Locate every blood parasite and identify its species.
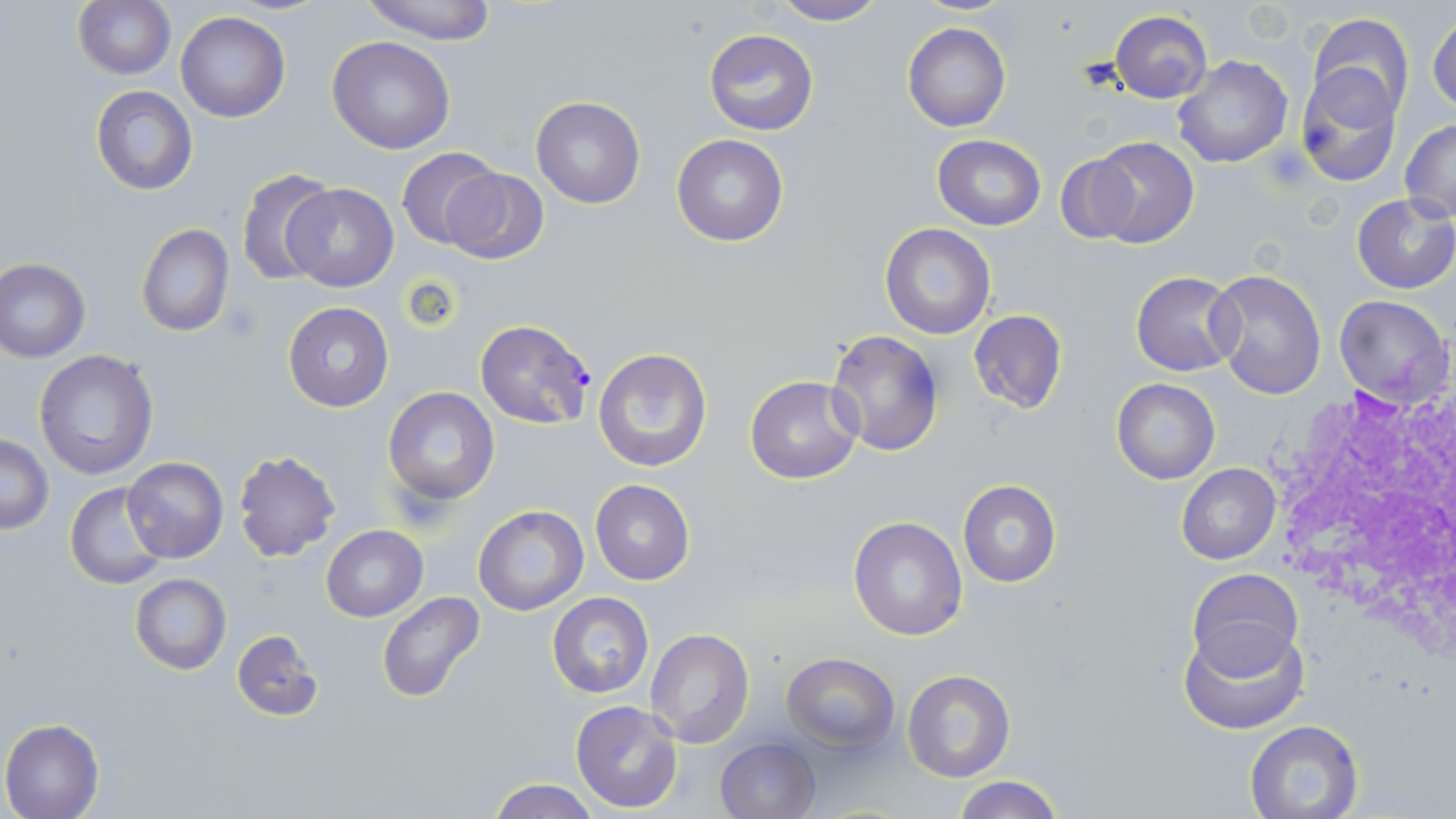
Approximate bounding boxes as (x1,y1)-(x2,y2) corner pairs in pixels.
Plasmodium falciparum-infected red blood cells: (475,319)-(595,429).
No Plasmodium ovale, Plasmodium malariae, Plasmodium vivax, Babesia divergens, or Trypanosoma brucei observed.

Platelet locations: (222,298)-(263,342). White blood cell locations: (1262,379)-(1456,641). Uninfected red blood cell locations: (360,0)-(500,43), (72,1)-(175,79), (767,1)-(891,26), (1428,10)-(1456,115), (175,12)-(291,122), (1109,12)-(1212,103), (1307,12)-(1415,120), (903,22)-(1011,131), (703,30)-(819,135), (327,36)-(455,154), (1172,55)-(1292,169), (1295,66)-(1402,187), (90,86)-(198,195), (531,96)-(645,209), (1399,119)-(1456,222), (671,134)-(788,247), (932,134)-(1046,230), (1086,134)-(1200,248), (398,147)-(500,249), (1056,155)-(1141,243), (236,167)-(336,286), (442,167)-(548,265), (283,183)-(400,293), (1352,194)-(1456,294), (880,222)-(996,339), (136,224)-(235,338), (0,257)-(92,362), (1207,269)-(1325,398), (1130,271)-(1241,375), (1334,293)-(1453,408), (283,302)-(394,412), (967,310)-(1068,416), (825,329)-(945,458), (591,346)-(714,474), (34,349)-(159,479), (745,375)-(864,485), (1111,378)-(1219,484), (383,387)-(500,505), (1,435)-(54,534), (232,450)-(342,564), (123,457)-(228,563), (1176,463)-(1281,565), (590,479)-(694,585), (957,480)-(1062,588), (65,482)-(170,590), (473,505)-(588,615), (847,515)-(968,641), (320,525)-(428,621), (1189,566)-(1301,671), (129,573)-(231,674), (376,592)-(487,705), (548,592)-(653,698), (1177,621)-(1308,735), (646,628)-(755,747), (231,630)-(322,721), (781,653)-(900,752), (901,669)-(1015,783), (570,700)-(686,814), (0,719)-(104,819), (1244,719)-(1366,819), (715,737)-(821,819), (949,776)-(1068,819), (486,778)-(601,819). Slide-level diagnosis: Plasmodium falciparum. 1000x magnification. Thin blood film. Optical microscopy. Image is 1456×819 pixels. Single field of view. May-Grünwald-Giemsa-stained preparation.